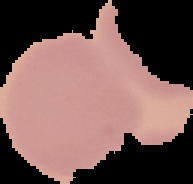
Summary:
  - Image size: 193×184 pixels
  - Preparation: thin blood smear
  - Result: no Plasmodium parasites detected
  - Image type: segmented cell region on a black background